Locate and identify every blood parasite.
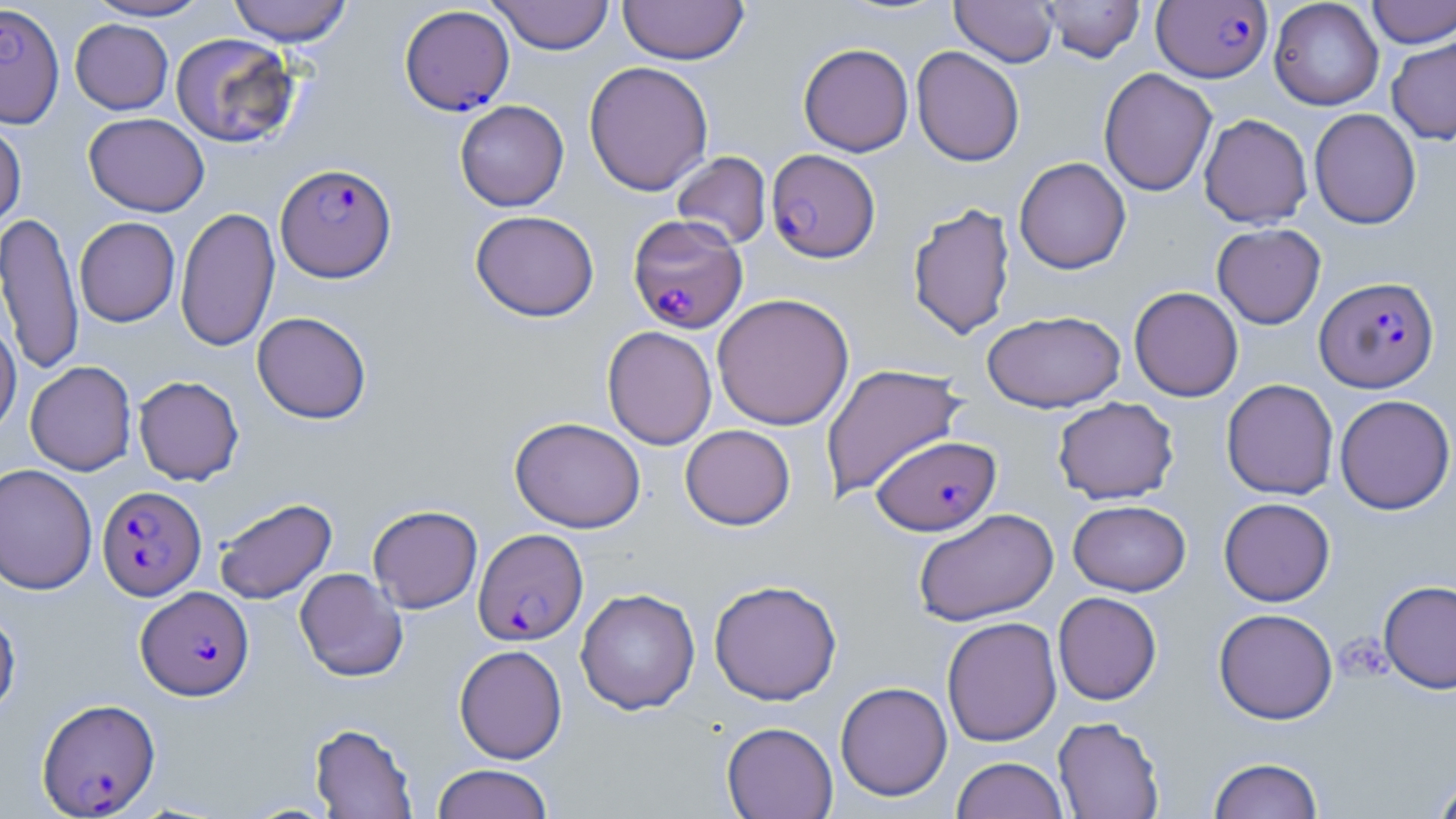
Approximate bounding boxes as (x1,y1)-(x2,y2) corner pairs in pixels.
Plasmodium falciparum-infected red blood cells: (1153,1)-(1272,83), (0,3)-(65,128), (399,5)-(514,115), (766,148)-(881,263), (275,163)-(397,282), (627,214)-(748,333), (1315,276)-(1439,393), (872,435)-(1001,535), (97,485)-(206,600), (473,528)-(588,645), (136,586)-(254,701), (37,698)-(160,817).
No Plasmodium ovale, Plasmodium malariae, Plasmodium vivax, Babesia divergens, or Trypanosoma brucei observed.

Uninfected red blood cell locations: (84,0)-(213,21), (227,0)-(353,45), (489,0)-(614,55), (618,0)-(749,65), (951,0)-(1058,67), (1365,0)-(1455,48), (1040,1)-(1144,63), (1269,1)-(1384,110), (70,18)-(173,115), (170,32)-(300,148), (1386,37)-(1456,145), (798,43)-(914,156), (911,46)-(1025,166), (584,61)-(714,196), (1098,67)-(1217,196), (454,100)-(569,211), (1309,109)-(1421,229), (84,112)-(209,217), (1199,113)-(1312,228), (0,118)-(26,230), (671,151)-(771,250), (1013,157)-(1131,274), (907,202)-(1016,340), (175,206)-(280,352), (470,210)-(599,322), (0,211)-(84,377), (75,217)-(180,327), (1212,223)-(1326,329), (1129,286)-(1244,402), (712,293)-(854,430), (981,310)-(1125,412), (252,311)-(372,424), (0,316)-(21,438), (602,326)-(718,450), (25,361)-(136,476), (820,363)-(967,500), (133,375)-(244,485), (1221,378)-(1339,499), (1334,394)-(1455,515), (1053,396)-(1179,504), (509,416)-(646,533), (680,424)-(795,530), (0,463)-(98,595), (214,497)-(337,604), (1219,497)-(1335,606), (1068,500)-(1191,596), (368,505)-(482,613), (913,508)-(1059,626), (294,567)-(408,682), (708,579)-(843,705), (1378,580)-(1456,693), (576,588)-(700,714), (1053,592)-(1162,705), (0,606)-(21,721), (1214,608)-(1338,724), (941,616)-(1062,747), (454,644)-(568,764), (835,681)-(952,801), (1053,716)-(1165,819), (721,721)-(838,818), (310,722)-(418,818), (951,756)-(1068,819), (1208,756)-(1324,818), (431,763)-(554,819), (1431,774)-(1456,819). Slide-level diagnosis: Plasmodium falciparum. May-Grünwald-Giemsa stain. One field of a larger specimen. Thin blood film. Optical microscopy. Image is 1456×819 pixels. 1000x magnification.